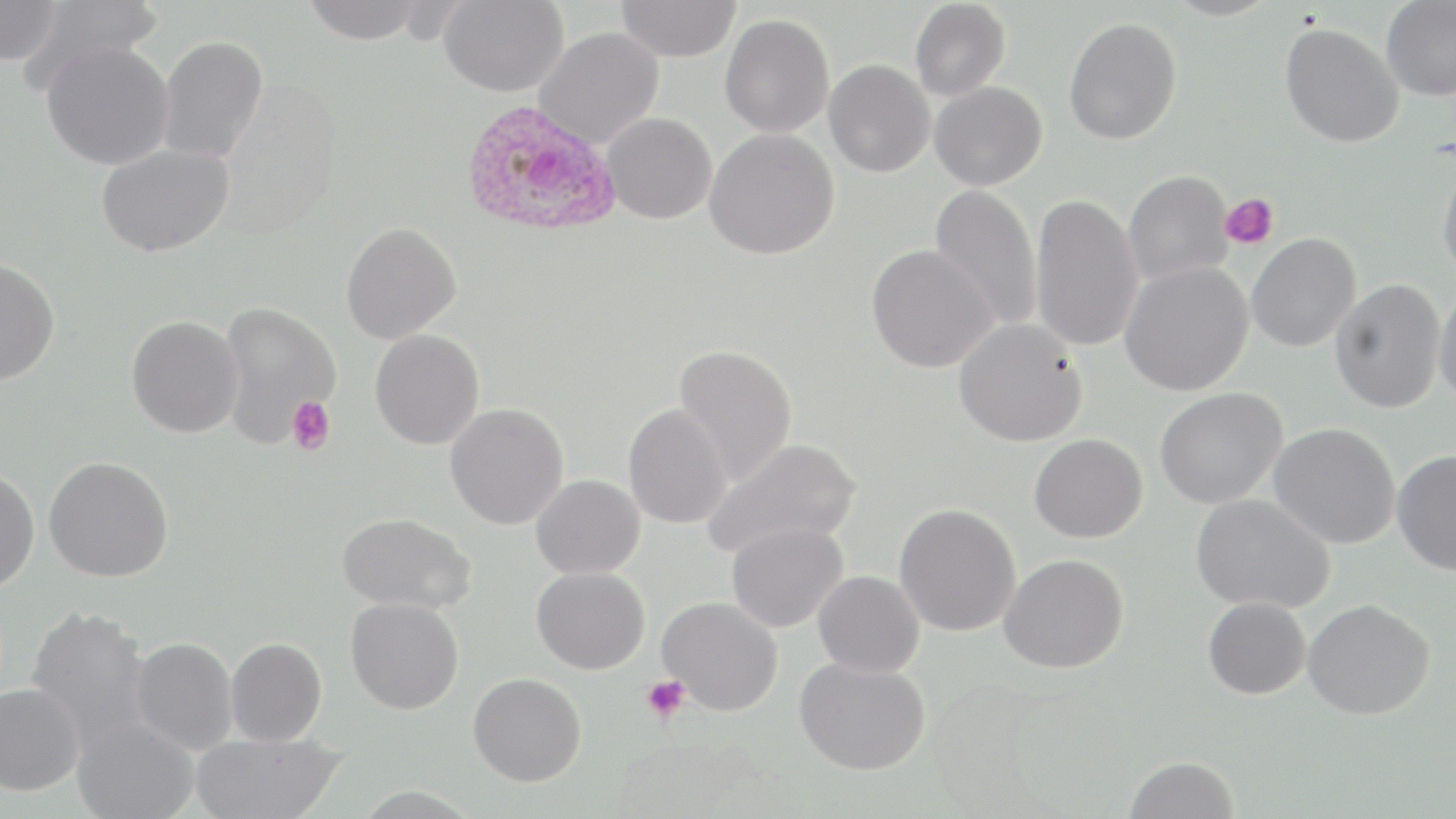

Summary:
  - Coordinate format: approximate bounding boxes as (x1, y1, x2, y2) in pixels
  - Plasmodium ovale-infected red blood cell locations: (460, 99, 621, 238)
  - Platelet locations: (1218, 192, 1279, 250), (287, 396, 336, 456), (640, 675, 691, 722)
  - Uninfected red blood cell locations: (299, 0, 428, 44), (439, 0, 568, 98), (1380, 0, 1456, 101), (0, 1, 64, 66), (19, 1, 163, 94), (615, 1, 742, 63), (909, 1, 1010, 101), (719, 13, 834, 138), (1063, 17, 1182, 145), (1280, 23, 1404, 148), (534, 27, 664, 149), (157, 35, 269, 164), (41, 40, 175, 170), (824, 59, 935, 178), (929, 81, 1047, 191), (601, 112, 717, 224), (704, 127, 839, 260), (96, 142, 234, 257), (1437, 165, 1456, 282), (1123, 170, 1234, 286), (929, 184, 1042, 332), (1030, 192, 1143, 353), (341, 222, 462, 344), (1247, 233, 1361, 352), (865, 244, 999, 372), (0, 258, 60, 385), (1120, 262, 1254, 396), (1330, 278, 1446, 413), (1434, 284, 1456, 411), (217, 301, 341, 447), (126, 315, 243, 438), (953, 318, 1088, 447), (370, 329, 484, 450), (673, 343, 797, 485), (1154, 387, 1288, 509), (444, 402, 569, 530), (622, 404, 732, 529), (1268, 423, 1401, 550), (1029, 433, 1148, 543), (701, 437, 862, 560), (1391, 449, 1456, 577), (44, 455, 174, 582), (0, 468, 40, 592), (531, 474, 645, 579), (1190, 493, 1336, 614), (894, 502, 1021, 637), (337, 512, 476, 614), (725, 520, 849, 633), (999, 553, 1129, 674), (532, 567, 650, 675), (813, 570, 925, 678), (657, 596, 784, 716), (345, 597, 464, 715), (1202, 597, 1311, 699), (1303, 599, 1435, 720), (24, 605, 152, 750), (130, 637, 238, 755), (225, 637, 328, 746), (794, 657, 931, 775), (468, 672, 587, 786), (0, 682, 85, 796), (71, 715, 201, 819), (190, 731, 344, 819), (1123, 756, 1239, 818)
  - Slide-level diagnosis: Plasmodium ovale
  - Magnification: 1000x
  - Image size: 1456×819 pixels
  - Stain: May-Grünwald-Giemsa
  - Modality: light microscopy
  - Preparation: thin blood film
  - Field of view: one of a larger specimen